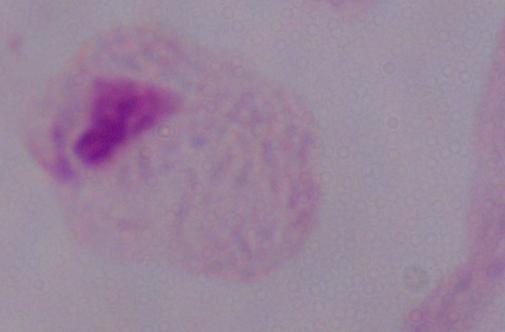
A trichomonad is seen. Photomicrograph. Captured at 1000x magnification.